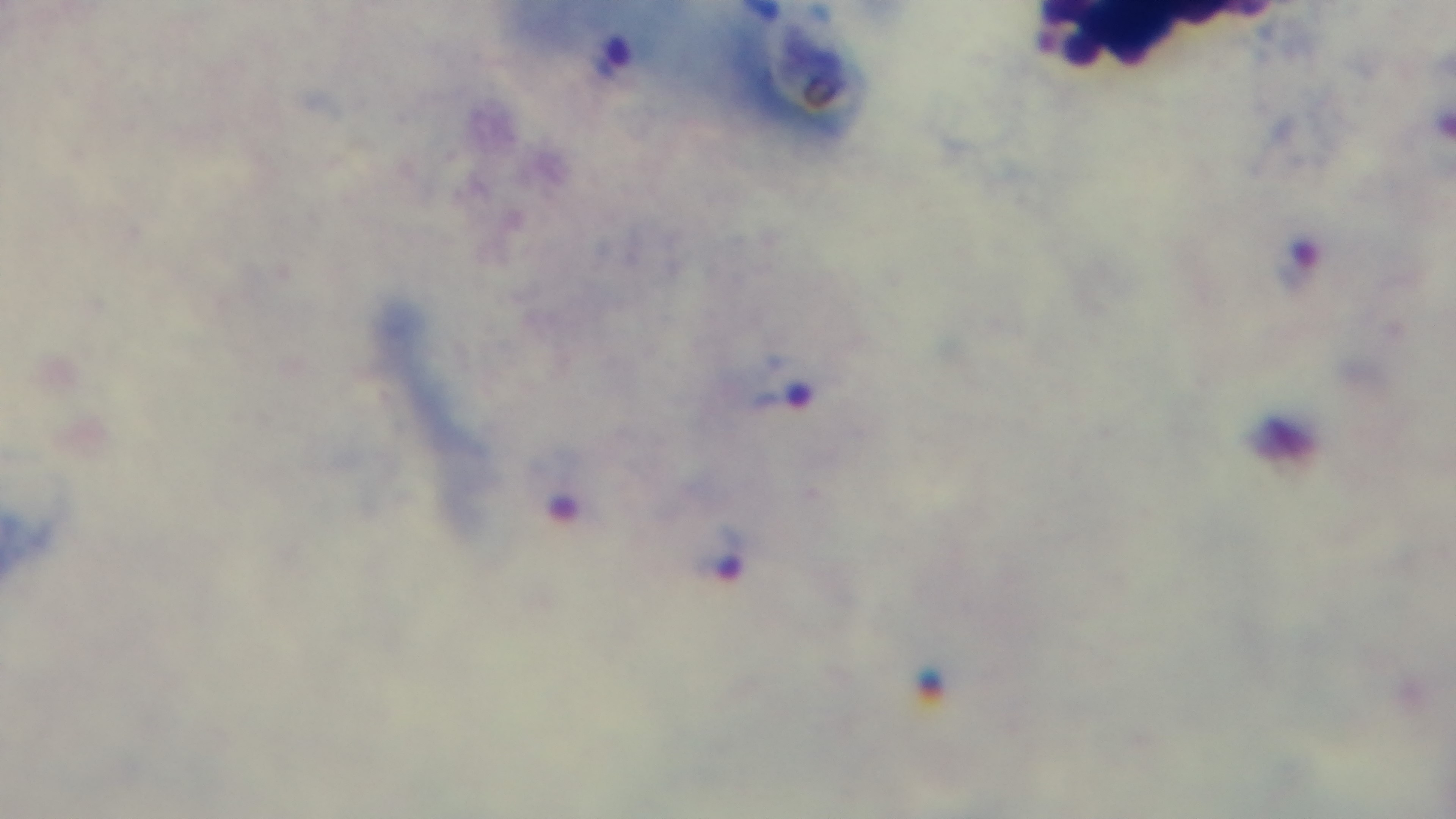

{
  "malaria_status": "infected",
  "capture": "mounted 4K digital camera",
  "stain": "Giemsa",
  "field_of_view": "single",
  "objective": "100x oil immersion",
  "preparation": "thick smear",
  "modality": "light microscopy"
}